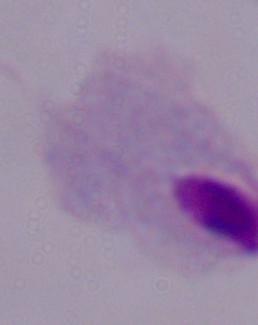

Captured at 1000x magnification. Micrograph. A trichomonad is shown.